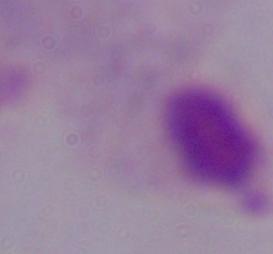
Summary:
  - Identification: trichomonad
  - Magnification: 1000x
  - Modality: photomicrograph